Assess the morphology of the erythrocytes.
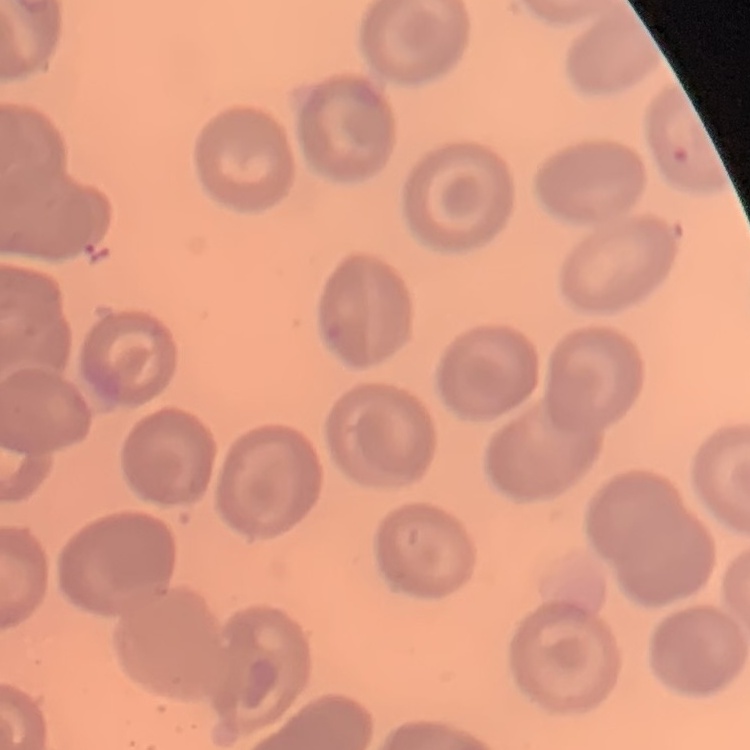

No rouleaux formation.

One tile cut from a larger photomicrograph. Thin blood smear. Field's or Giemsa stain.